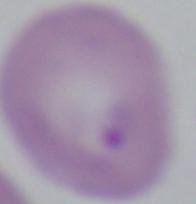

identification = Babesia
modality = micrograph
magnification = 1000x